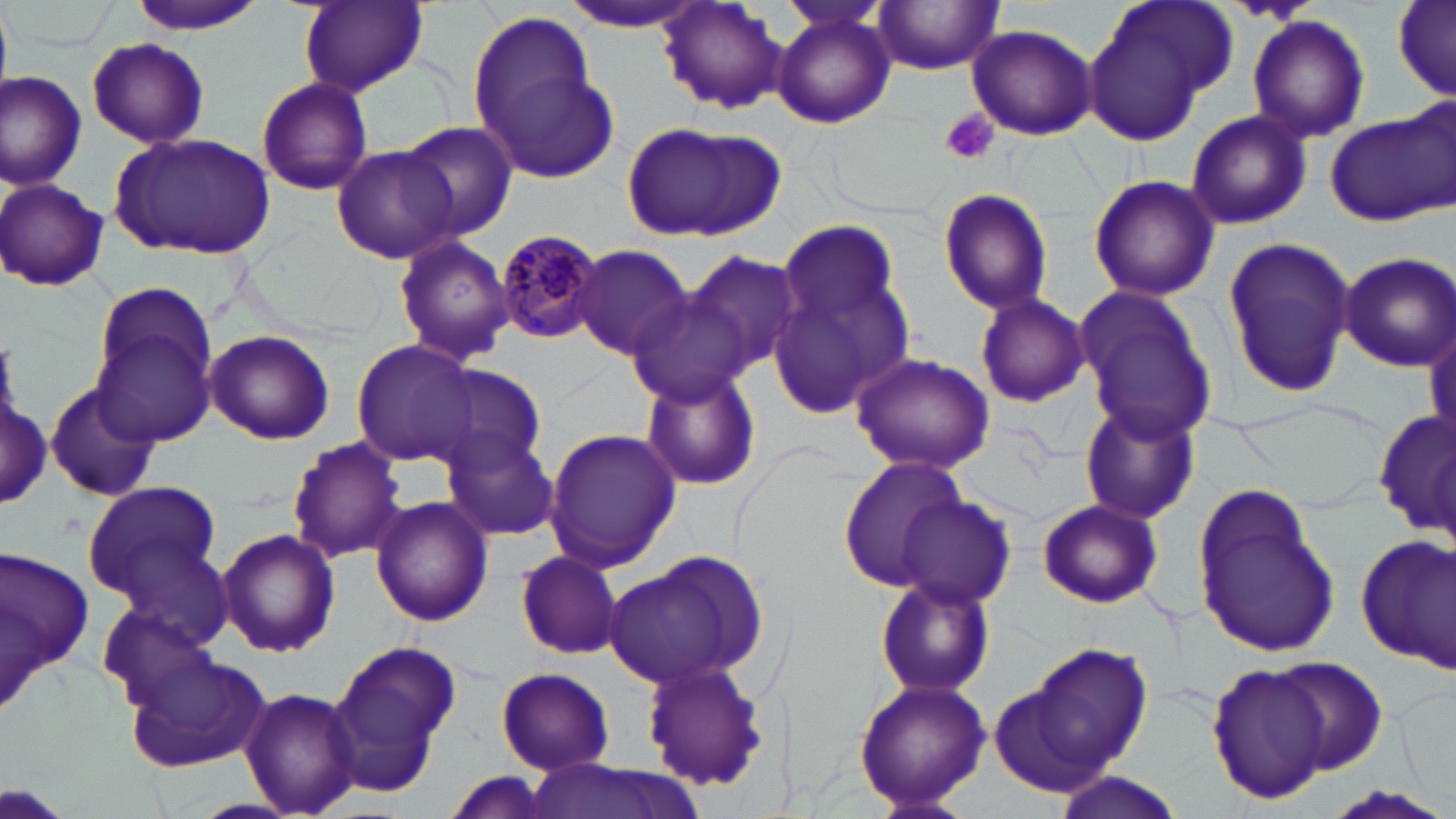
Summary:
  - Coordinate format: approximate bounding boxes as (x1,y1)-(x2,y2) corner pairs in pixels
  - Platelet locations: (939,109)-(999,165)
  - Uninfected red blood cell locations: (130,0)-(265,35), (297,0)-(428,97), (560,0)-(709,31), (655,0)-(789,117), (1082,0)-(1237,145), (1391,0)-(1455,104), (873,1)-(1004,74), (770,8)-(896,128), (467,9)-(606,154), (1246,18)-(1371,141), (964,24)-(1099,140), (85,37)-(210,149), (481,63)-(623,187), (0,71)-(87,189), (256,76)-(374,196), (1184,110)-(1312,231), (1324,110)-(1451,227), (397,121)-(517,242), (621,121)-(785,242), (110,130)-(278,260), (331,145)-(458,264), (1087,173)-(1220,302), (1,178)-(111,293), (935,185)-(1054,317), (771,219)-(914,413), (393,234)-(514,364), (1220,236)-(1356,398), (569,244)-(695,358), (681,250)-(806,379), (1335,251)-(1455,370), (87,282)-(221,446), (1071,284)-(1219,444), (624,289)-(755,404), (974,294)-(1091,408), (1424,314)-(1455,445), (203,330)-(335,445), (351,339)-(480,467), (848,351)-(996,474), (428,365)-(547,475), (638,366)-(763,492), (44,381)-(161,503), (1,383)-(49,512), (1075,396)-(1202,526), (1235,399)-(1394,508), (1375,407)-(1454,541), (543,426)-(681,573), (443,432)-(561,542), (287,437)-(406,564), (835,455)-(971,594), (1189,479)-(1338,662), (81,480)-(222,604), (894,493)-(1015,609), (370,496)-(493,627), (1034,498)-(1164,609), (218,528)-(339,657), (1357,532)-(1455,673), (0,542)-(95,703), (606,547)-(772,691), (513,549)-(624,659), (875,574)-(995,700), (98,604)-(224,711), (326,640)-(462,791), (1008,641)-(1158,786), (122,647)-(271,774), (1264,656)-(1390,775), (639,658)-(770,793), (1206,663)-(1334,804), (494,667)-(615,774), (852,678)-(990,810), (238,686)-(364,818), (523,761)-(706,819), (441,773)-(554,819), (1049,773)-(1184,819), (1320,786)-(1453,819)
  - Plasmodium malariae-infected red blood cell locations: (492,227)-(604,343)
  - Slide-level diagnosis: Plasmodium malariae
  - Preparation: thin blood smear
  - Magnification: 1000x
  - Modality: light microscopy
  - Stain: May-Grünwald-Giemsa
  - Image size: 1456×819 pixels
  - Field of view: one of a larger specimen